Name the parasite shown.
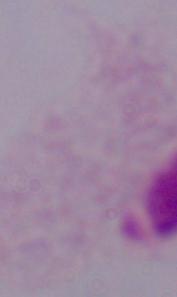

This is a trichomonad.

1000x magnification. Micrograph.